Identify the parasite.
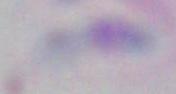
This is Toxoplasma gondii.

1000x magnification. Micrograph.